Assess the morphology of the red blood cells.
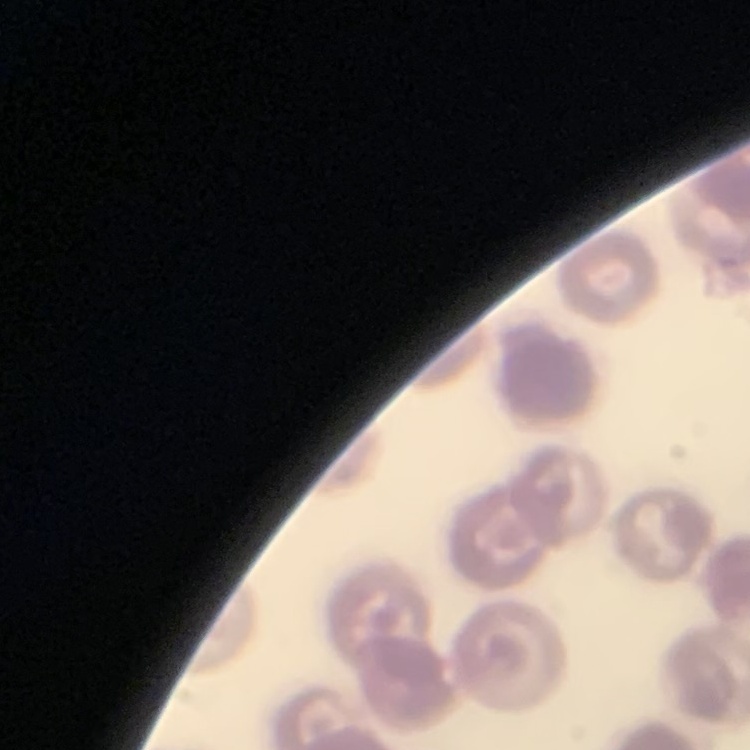
No rouleaux formation.

Summary:
  - Image type: one tile cut from a larger photomicrograph
  - Stain: Field's or Giemsa
  - Preparation: thin blood smear